Point out each malaria parasite.
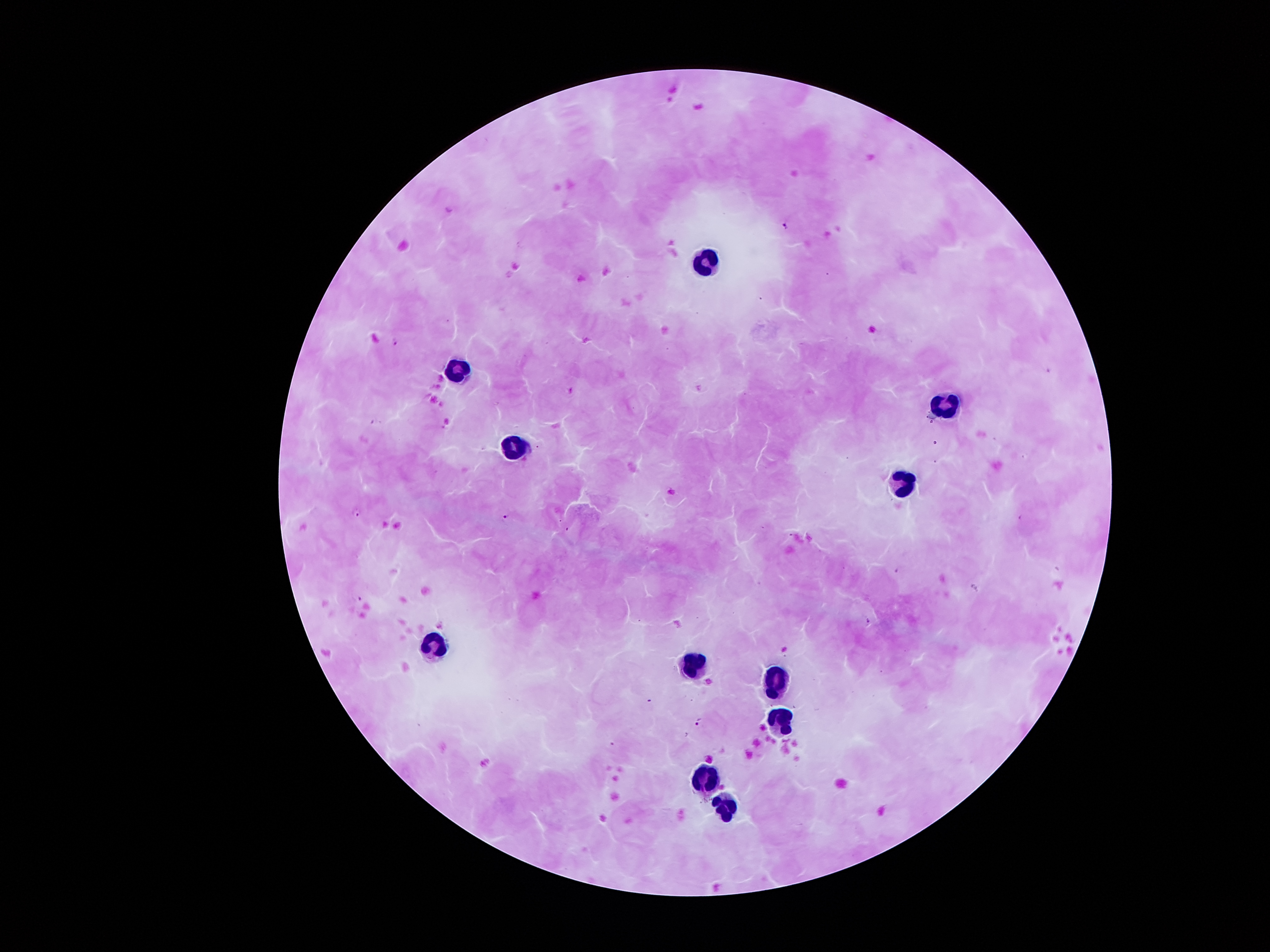
Approximate centers as (x, y) in pixels.
Malaria parasites: (786, 225), (395, 342), (570, 391), (357, 515), (506, 520), (358, 598), (699, 721).

Leukocyte locations: (703, 262), (457, 370), (947, 407), (508, 448), (906, 477), (433, 643), (692, 662), (777, 680), (778, 720), (706, 775), (726, 806). Giemsa stain. Patient malaria status: infected with Plasmodium falciparum. 100x magnification. Thick peripheral-blood smear. Smartphone photograph taken through the microscope eyepiece. Image is 1270×952 pixels. Single field of view.